Name the blood parasite species.
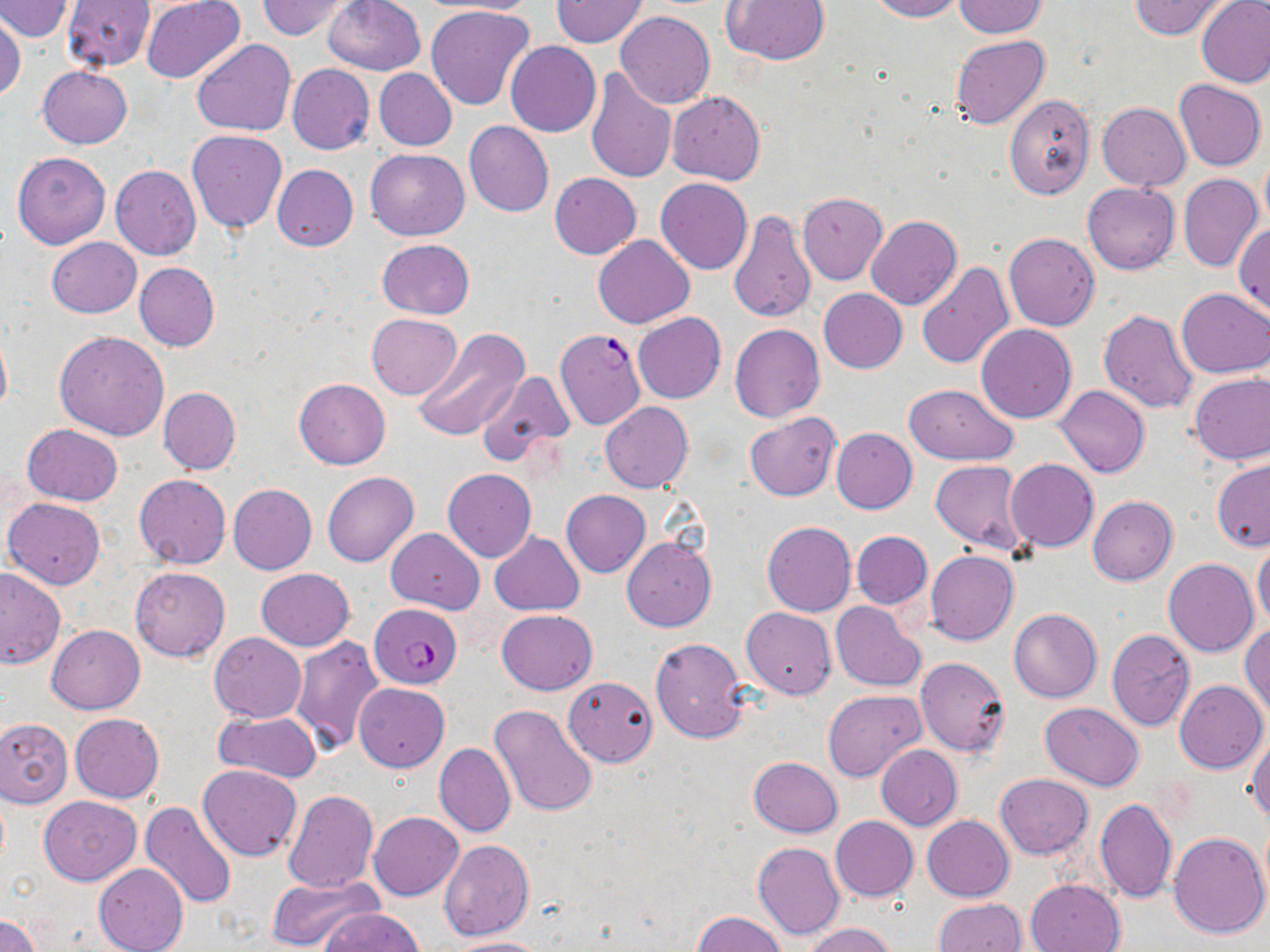

Plasmodium falciparum.

Summary:
  - Coordinate format: approximate bounding boxes as [x1, y1, x2, y2] in pixels
  - Plasmodium falciparum-infected red blood cell locations: [555, 327, 646, 429], [370, 603, 463, 689]
  - Uninfected red blood cell locations: [2, 0, 76, 39], [141, 0, 247, 85], [256, 0, 351, 40], [323, 0, 426, 75], [422, 0, 541, 16], [721, 0, 831, 66], [866, 0, 963, 21], [954, 0, 1047, 38], [1130, 0, 1231, 39], [61, 1, 154, 70], [551, 1, 647, 48], [1196, 1, 1270, 87], [425, 5, 535, 112], [614, 11, 715, 109], [0, 12, 25, 104], [950, 34, 1050, 129], [191, 38, 295, 137], [505, 41, 601, 137], [287, 64, 375, 155], [38, 66, 131, 148], [584, 67, 677, 184], [374, 69, 457, 151], [1174, 80, 1266, 170], [667, 91, 765, 184], [1003, 94, 1095, 199], [1097, 103, 1190, 190], [465, 122, 554, 216], [186, 129, 288, 234], [366, 148, 470, 241], [12, 152, 110, 250], [1259, 154, 1270, 231], [273, 164, 358, 252], [110, 165, 201, 260], [550, 173, 641, 259], [1178, 174, 1262, 272], [656, 179, 752, 275], [1082, 182, 1180, 274], [797, 192, 887, 285], [727, 209, 816, 321], [866, 215, 961, 310], [1234, 223, 1270, 317], [1004, 232, 1100, 330], [593, 235, 694, 328], [46, 237, 142, 318], [377, 239, 474, 320], [134, 262, 220, 350], [917, 263, 1014, 369], [818, 287, 907, 372], [1177, 288, 1270, 378], [1099, 309, 1199, 413], [632, 312, 726, 404], [367, 313, 462, 399], [730, 323, 825, 423], [976, 323, 1077, 423], [0, 324, 12, 421], [413, 329, 528, 443], [55, 331, 169, 441], [477, 370, 575, 463], [1189, 371, 1270, 465], [294, 378, 391, 469], [904, 383, 1019, 464], [1055, 385, 1150, 478], [159, 387, 240, 475], [601, 401, 693, 493], [746, 413, 840, 501], [23, 424, 123, 505], [831, 428, 919, 514], [1005, 458, 1099, 551], [1213, 458, 1270, 552], [930, 460, 1030, 556], [443, 468, 536, 562], [322, 471, 419, 567], [133, 474, 232, 569], [229, 483, 316, 574], [561, 490, 651, 577], [1088, 495, 1178, 585], [5, 497, 105, 590], [762, 521, 856, 617], [386, 528, 484, 613], [852, 531, 933, 608], [490, 532, 584, 615], [622, 537, 716, 630], [1253, 542, 1270, 631], [925, 550, 1019, 646], [1165, 559, 1258, 657], [130, 565, 230, 662], [0, 568, 65, 669], [256, 568, 355, 651], [830, 601, 925, 692], [742, 607, 837, 699], [497, 609, 597, 694], [1009, 609, 1101, 702], [47, 624, 145, 714], [1240, 624, 1269, 718], [1107, 629, 1196, 730], [209, 632, 306, 723], [290, 636, 385, 755], [650, 637, 749, 743], [914, 656, 1010, 757], [563, 675, 658, 766], [1174, 680, 1268, 774], [355, 682, 449, 771], [823, 689, 926, 781], [1040, 702, 1144, 790], [490, 705, 599, 818], [215, 710, 322, 783], [70, 713, 164, 803], [0, 718, 72, 807], [1246, 723, 1270, 822], [434, 743, 514, 837], [876, 745, 963, 830], [749, 757, 843, 837], [197, 765, 303, 861], [994, 773, 1093, 859], [281, 790, 377, 894], [38, 795, 142, 885], [1094, 797, 1179, 904], [141, 801, 238, 911], [369, 812, 464, 901], [922, 814, 1014, 900], [831, 816, 918, 900], [1167, 830, 1269, 938], [438, 840, 534, 942], [753, 843, 845, 942], [94, 862, 189, 952], [264, 871, 380, 951], [1025, 878, 1125, 952], [933, 897, 1026, 951], [324, 909, 424, 952], [692, 911, 788, 952], [0, 915, 40, 952], [803, 923, 900, 952], [445, 936, 553, 952]
  - Image size: 1270×952 pixels
  - Magnification: 1000x
  - Stain: May-Grünwald-Giemsa
  - Preparation: thin blood film
  - Modality: optical microscopy
  - Field of view: single